Assess the morphology of the red blood cells.
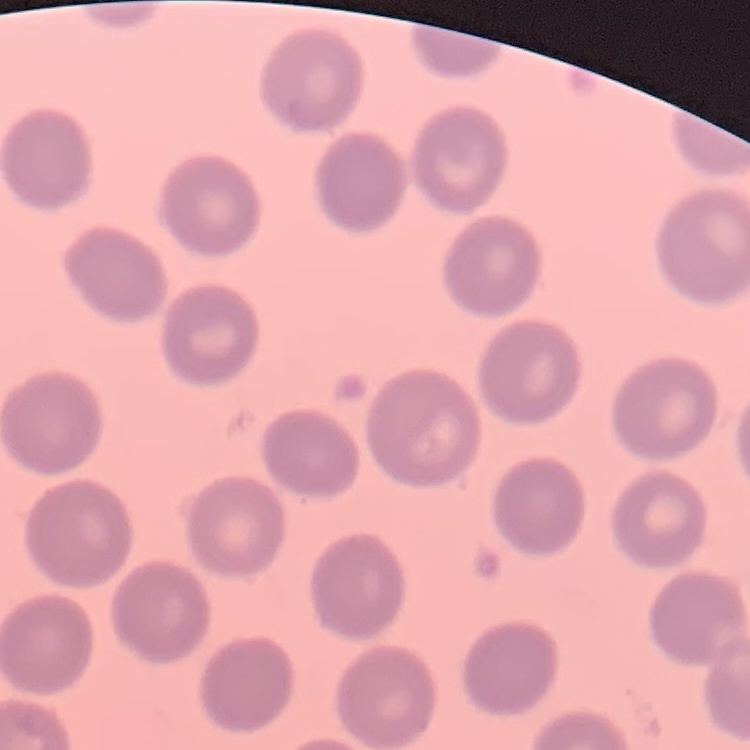

No rouleaux formation.

Summary:
  - Stain: Field's or Giemsa
  - Image type: one tile cut from a larger photomicrograph
  - Preparation: thin blood film